State which parasite is depicted.
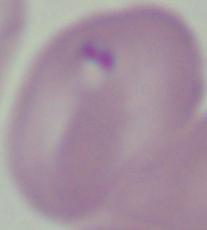

This is Babesia.

modality = photomicrograph
magnification = 1000x